Name the cell type shown.
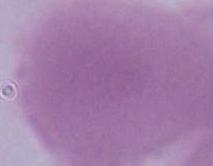
An erythrocyte.

{
  "magnification": "1000x",
  "modality": "micrograph"
}